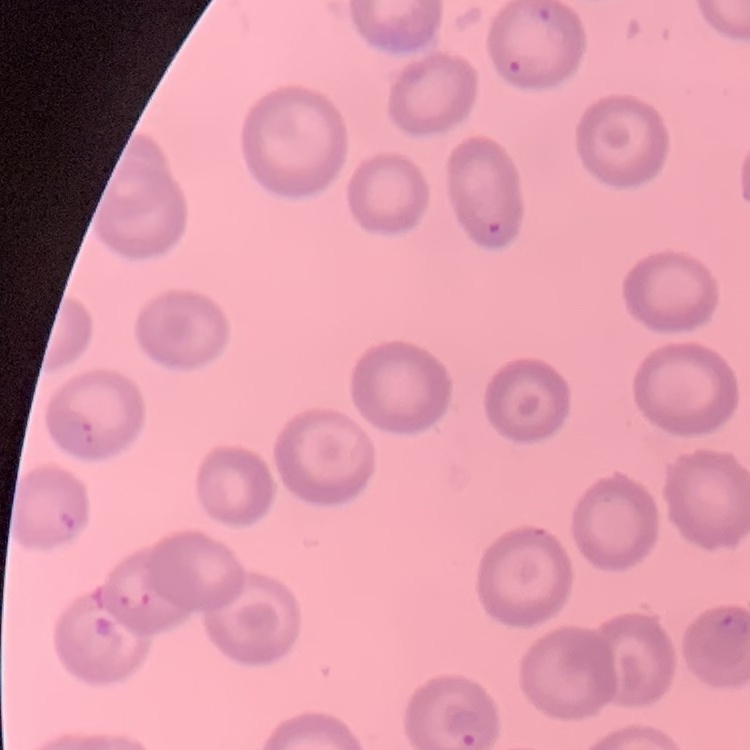
Summary:
  - Red blood cell morphology: no rouleaux formation
  - Stain: Field's or Giemsa
  - Image type: square crop of a larger photomicrograph
  - Preparation: thin peripheral smear